Point out each malaria parasite.
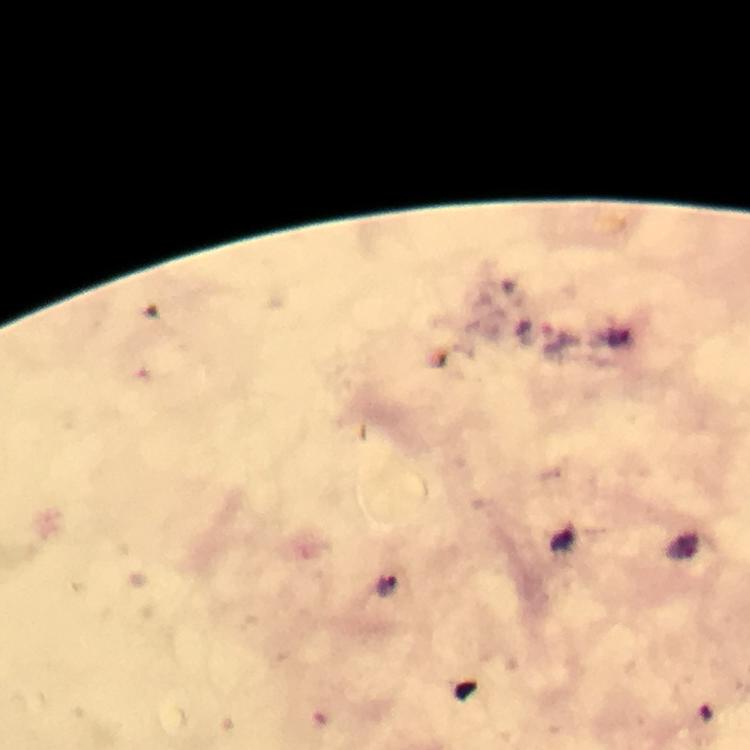

Approximate centers as {x, y} in pixels.
Malaria parasites: {387, 584}.

magnification: 100x
stain: Giemsa
capture: smartphone camera through the microscope
image_size: 750×750 pixels
cropped_from: one field of view
context: from a malaria diagnostic workup
immersion_oil: used
preparation: thick blood smear